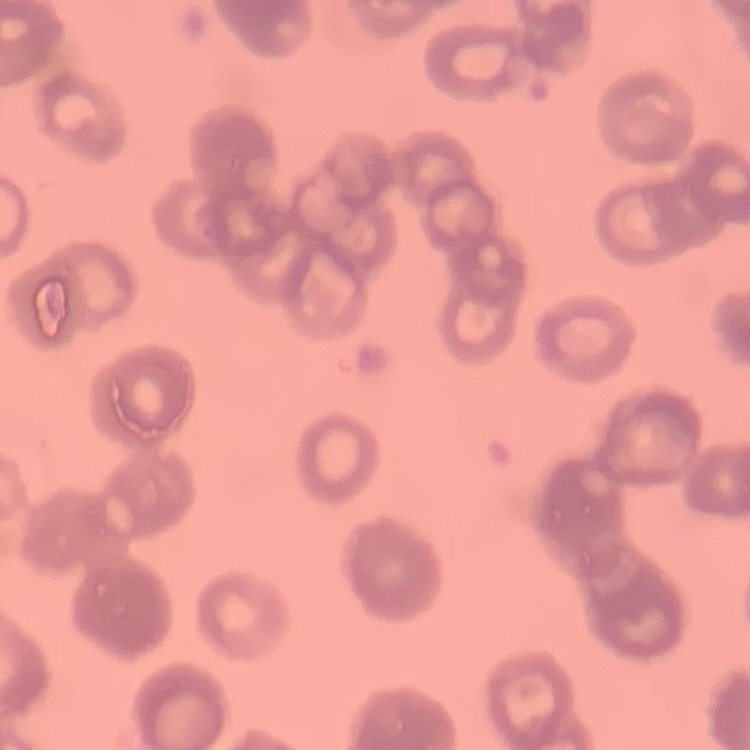

Summary:
  - Red blood cell morphology: rouleaux formation
  - Stain: Field's or Giemsa
  - Image type: square crop of a larger photomicrograph
  - Preparation: thin blood film